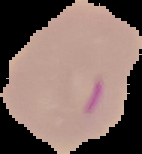

Summary:
  - Image size: 142×154 pixels
  - Preparation: thin blood film
  - Malaria status: parasitized
  - Image type: segmented cell region on a black background